Name the malaria species.
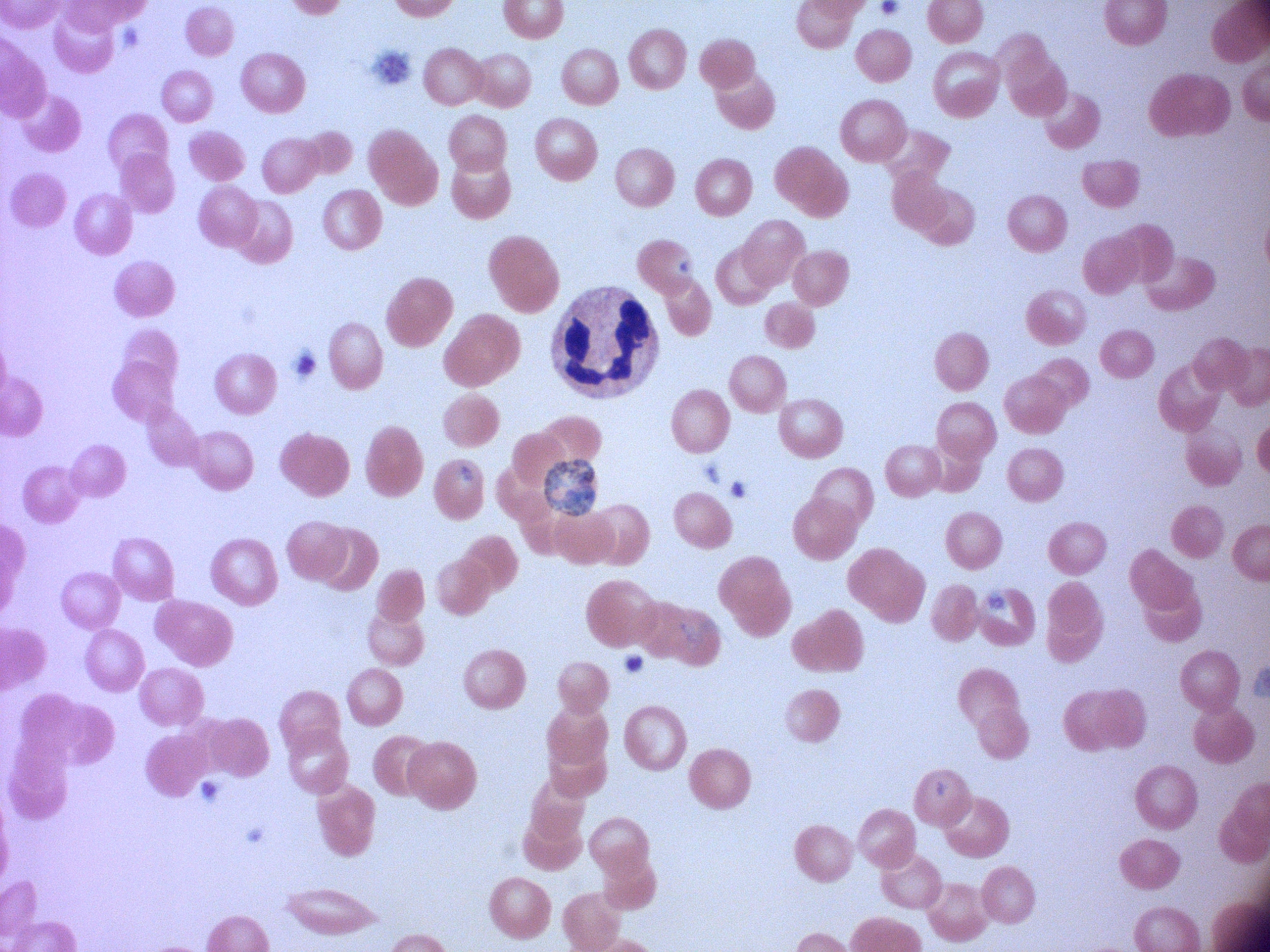
Plasmodium falciparum.

image size = 1270×952 pixels
magnification = 100x
field of view = single
preparation = thin blood film
schizont locations = approximate bounding boxes as (x1,y1)-(x2,y2) corner pairs in pixels, from the source annotation, which is not necessarily exhaustive: (544,459)-(595,516)
microscope = Leica DM2000 with built-in camera
stain = Giemsa